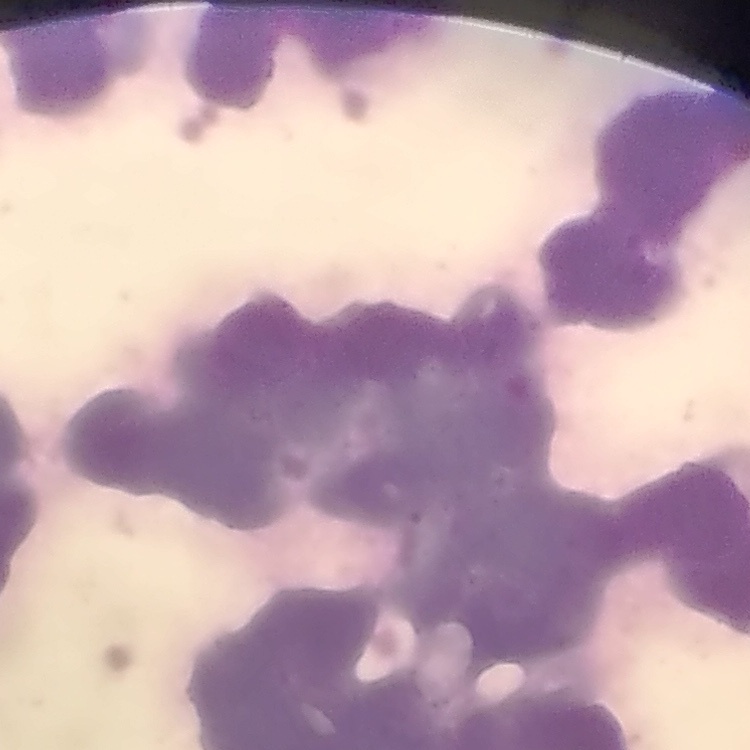

Summary:
  - Red blood cell morphology: rouleaux formation
  - Stain: Field's or Giemsa
  - Preparation: thin peripheral smear
  - Image type: one tile cut from a larger photomicrograph